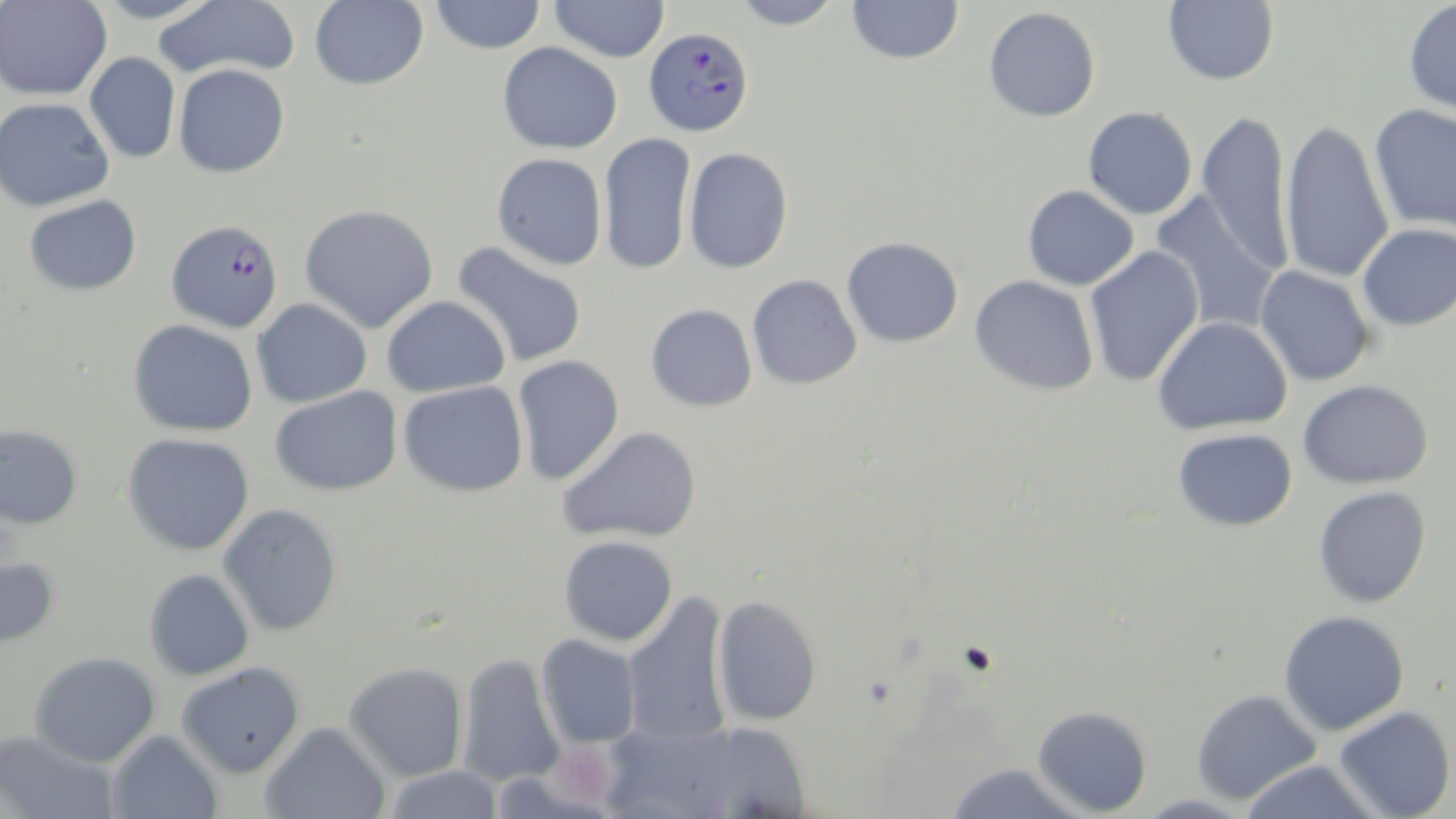

Summary:
  - Coordinate format: approximate bounding boxes as [x1, y1, x2, y2] in pixels
  - Plasmodium falciparum-infected red blood cell locations: [644, 26, 754, 136], [167, 219, 283, 332]
  - Platelet locations: [550, 742, 618, 808]
  - Uninfected red blood cell locations: [93, 0, 220, 24], [153, 0, 300, 81], [309, 0, 429, 90], [430, 0, 546, 54], [549, 0, 670, 62], [730, 0, 844, 29], [847, 0, 964, 64], [1163, 0, 1279, 85], [1403, 0, 1456, 118], [0, 1, 112, 101], [984, 6, 1100, 122], [497, 42, 622, 154], [85, 52, 180, 164], [174, 63, 290, 178], [0, 97, 114, 211], [1368, 103, 1456, 235], [1083, 106, 1197, 219], [1197, 109, 1294, 274], [1279, 118, 1394, 285], [598, 132, 697, 275], [683, 147, 793, 274], [491, 153, 607, 271], [1023, 185, 1139, 290], [1151, 191, 1282, 334], [24, 194, 142, 296], [300, 204, 438, 333], [1357, 224, 1456, 330], [842, 236, 963, 347], [451, 241, 588, 368], [1084, 245, 1205, 388], [1254, 265, 1375, 387], [747, 274, 863, 389], [970, 275, 1099, 395], [382, 295, 510, 397], [252, 298, 372, 408], [646, 303, 758, 412], [1153, 316, 1292, 434], [128, 319, 259, 437], [512, 355, 625, 485], [1298, 379, 1433, 489], [398, 381, 528, 497], [270, 386, 402, 496], [0, 424, 83, 529], [558, 425, 703, 544], [1173, 428, 1298, 531], [122, 432, 254, 555], [1313, 486, 1431, 608], [218, 503, 342, 636], [558, 535, 678, 647], [0, 554, 60, 649], [143, 568, 255, 680], [622, 591, 733, 747], [711, 594, 822, 727], [1278, 610, 1409, 736], [536, 633, 642, 749], [28, 651, 162, 768], [457, 652, 566, 787], [176, 662, 305, 778], [344, 662, 469, 781], [1192, 688, 1321, 805], [1032, 705, 1152, 816], [1334, 705, 1455, 819], [260, 721, 392, 819], [604, 721, 741, 818], [695, 721, 812, 817], [0, 730, 120, 819], [106, 730, 224, 819], [1240, 760, 1383, 819], [945, 763, 1088, 819], [380, 765, 506, 818]
  - Slide-level diagnosis: Plasmodium falciparum
  - Image size: 1456×819 pixels
  - Stain: May-Grünwald-Giemsa
  - Magnification: 1000x
  - Modality: optical microscopy
  - Field of view: one of a larger specimen
  - Preparation: thin blood film